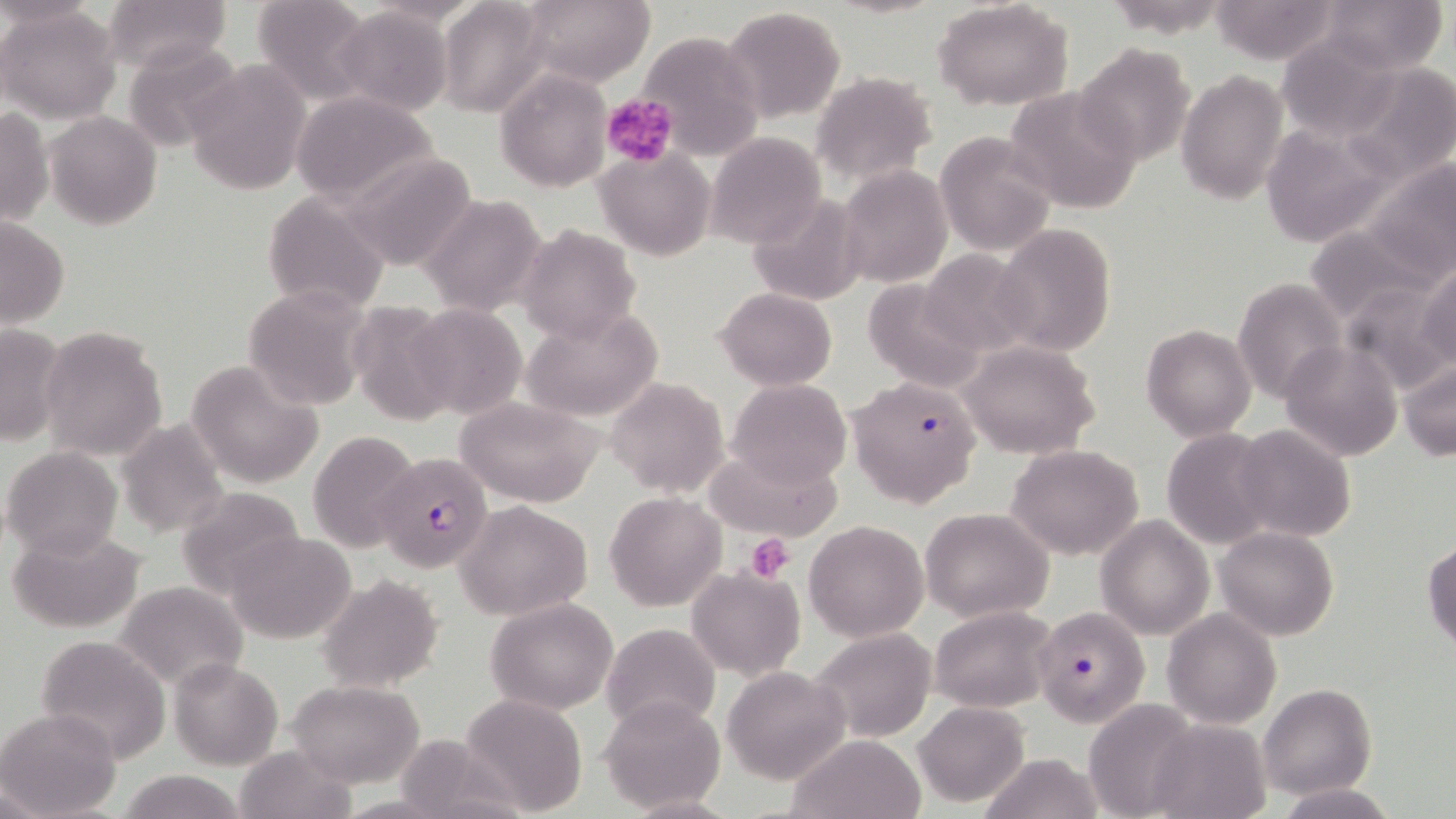
Approximate bounding boxes as (x1, y1, x2, y2) in pixels. Uninfected red blood cell locations: (101, 0, 233, 74), (252, 0, 375, 105), (933, 0, 1076, 111), (1208, 0, 1344, 64), (1317, 0, 1449, 75), (436, 1, 550, 118), (518, 1, 655, 88), (1, 5, 122, 123), (719, 5, 847, 121), (334, 6, 452, 114), (635, 29, 763, 159), (1276, 36, 1399, 141), (122, 40, 247, 154), (1075, 44, 1196, 166), (184, 61, 309, 195), (1339, 62, 1456, 186), (496, 70, 611, 192), (1175, 70, 1289, 205), (810, 72, 937, 188), (1004, 83, 1143, 215), (291, 90, 441, 206), (0, 106, 52, 227), (45, 111, 161, 229), (1257, 121, 1403, 246), (705, 131, 827, 247), (937, 132, 1056, 256), (338, 148, 479, 272), (594, 148, 715, 262), (1369, 159, 1456, 276), (837, 165, 953, 289), (262, 190, 390, 317), (746, 192, 868, 306), (421, 194, 548, 314), (0, 214, 69, 330), (994, 222, 1115, 360), (517, 223, 641, 346), (1303, 223, 1442, 329), (915, 249, 1038, 357), (1417, 262, 1456, 373), (861, 278, 990, 392), (1231, 278, 1347, 405), (1341, 284, 1455, 399), (716, 287, 837, 391), (242, 288, 372, 409), (347, 299, 460, 426), (405, 304, 526, 420), (520, 306, 663, 423), (0, 322, 66, 448), (1141, 323, 1257, 441), (37, 326, 169, 462), (958, 340, 1101, 459), (1278, 342, 1403, 461), (185, 359, 325, 487), (1399, 360, 1455, 460), (606, 377, 729, 495), (727, 378, 852, 489), (453, 396, 605, 507), (116, 419, 230, 539), (1229, 423, 1356, 542), (309, 429, 420, 554), (1160, 430, 1278, 549), (1007, 444, 1145, 561), (3, 445, 122, 560), (707, 454, 837, 539), (176, 486, 310, 598), (605, 491, 725, 610), (456, 500, 593, 621), (921, 507, 1055, 623), (1096, 515, 1214, 640), (803, 520, 929, 640), (7, 525, 148, 634), (1214, 527, 1340, 641), (221, 530, 357, 644), (1423, 538, 1455, 653), (686, 567, 806, 679), (317, 574, 443, 692), (112, 581, 249, 692), (486, 597, 619, 714), (929, 605, 1056, 711), (1163, 609, 1282, 728), (601, 622, 721, 737), (810, 628, 937, 743), (34, 636, 173, 760), (169, 656, 282, 769), (723, 665, 851, 783), (286, 679, 424, 786), (1260, 684, 1376, 800), (458, 691, 589, 817), (598, 694, 727, 811), (1085, 698, 1204, 817), (912, 700, 1030, 806), (0, 708, 120, 819), (1147, 719, 1273, 818), (785, 733, 925, 818), (390, 734, 525, 817), (233, 744, 358, 819), (980, 752, 1103, 819), (114, 770, 250, 819), (1274, 783, 1397, 819). Platelet locations: (601, 92, 678, 168), (745, 534, 795, 582). Plasmodium falciparum-infected red blood cell locations: (847, 374, 982, 507), (371, 442, 496, 566), (1034, 604, 1151, 726). Slide-level diagnosis: Plasmodium falciparum. Single field of view. May-Grünwald-Giemsa stain. 1000x magnification. Image is 1456×819 pixels. Thin blood film. Optical microscopy.